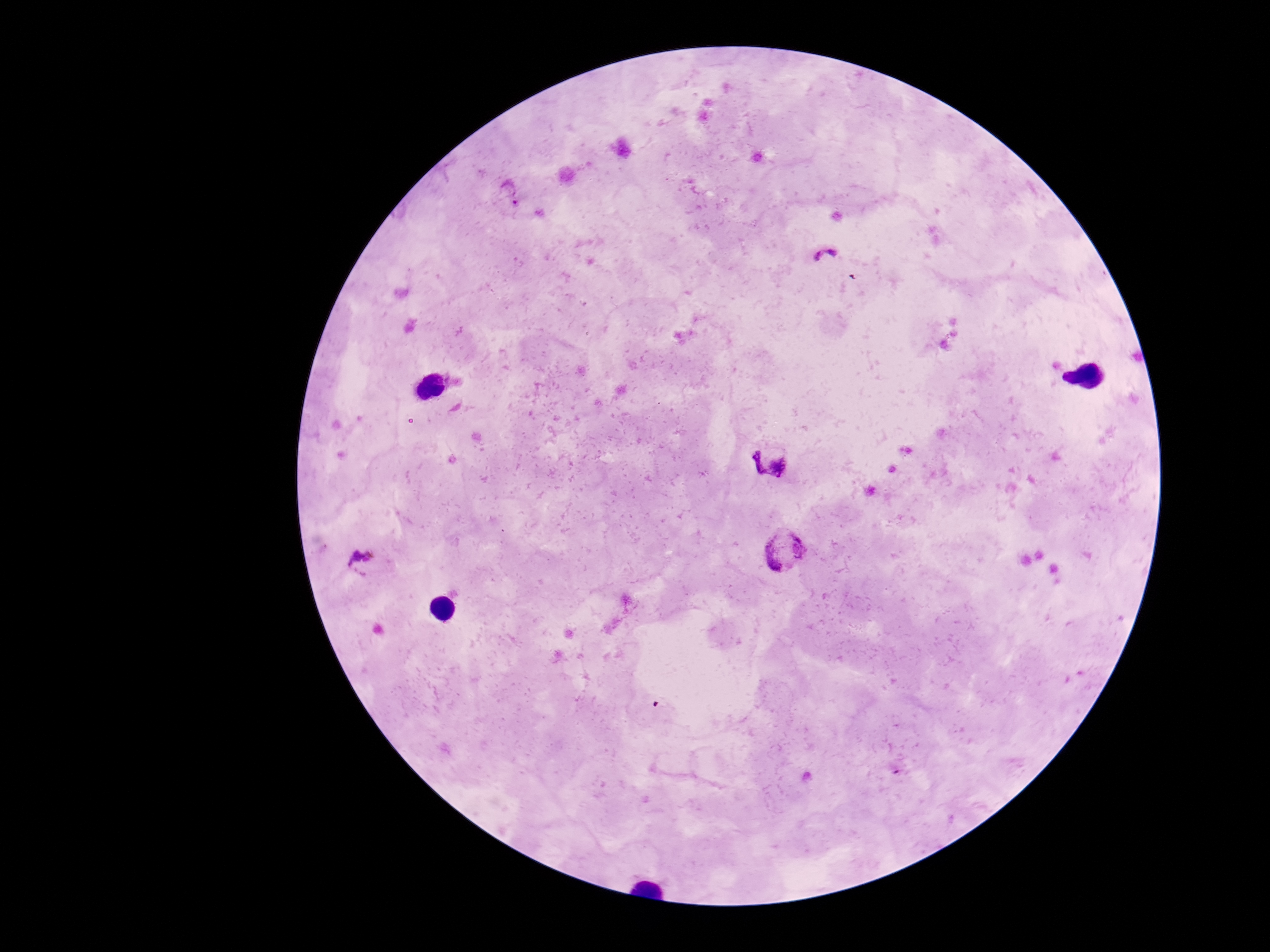
Approximate centers as {x, y} in pixels. Plasmodium parasite locations: {512, 192}, {825, 255}, {770, 461}, {787, 548}, {363, 563}. Photographed through the microscope eyepiece with a smartphone camera. Thick peripheral-blood smear. Patient malaria status: positive. Single field of view. Image is 1270×952 pixels. Giemsa stain. 100x magnification.